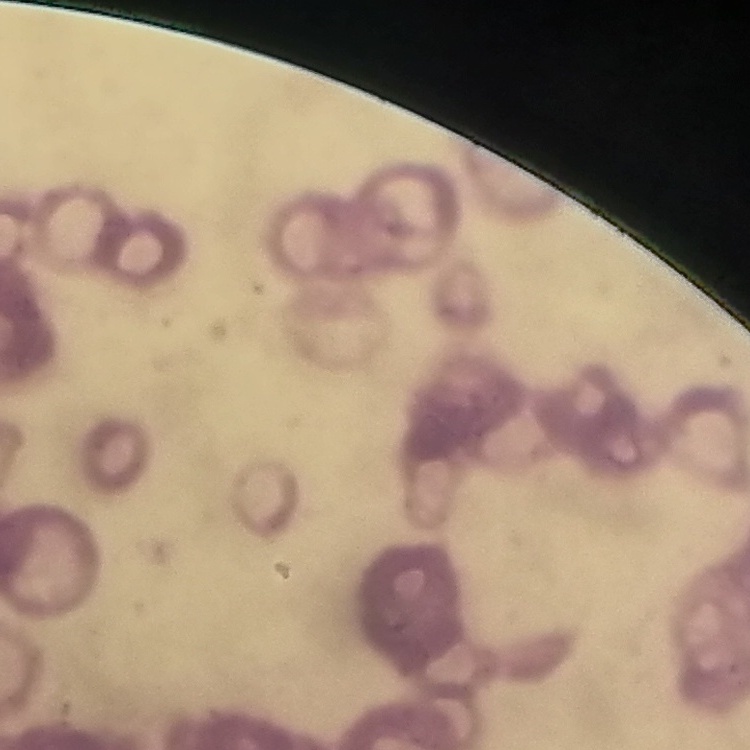

The red blood cells exhibit rouleaux formation. Square crop of a larger photomicrograph. Stained with either Field's or Giemsa. Thin peripheral smear.